Name the parasite shown.
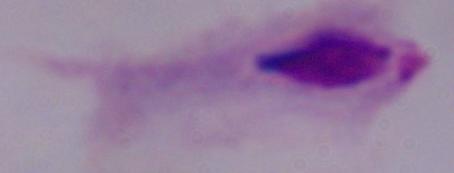

A trichomonad.

Photomicrograph. Captured at 1000x magnification.